Report the malaria status of this cell.
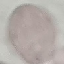
Uninfected.

stain = Giemsa
capture = smartphone camera at the microscope eyepiece
preparation = thin smear
image type = automatically extracted cell patch, resized to 64 × 64 pixels